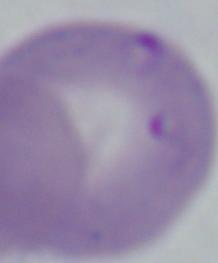

magnification = 1000x
identification = Babesia
modality = micrograph